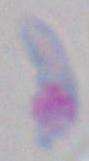

Summary:
  - Identification: Toxoplasma gondii
  - Modality: photomicrograph
  - Magnification: 1000x